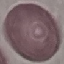
Malaria status: uninfected. Giemsa stain. Thin blood smear. Automatically extracted cell patch, resized to 64 × 64 pixels. Acquired by smartphone through the microscope eyepiece.